Name the blood parasite species.
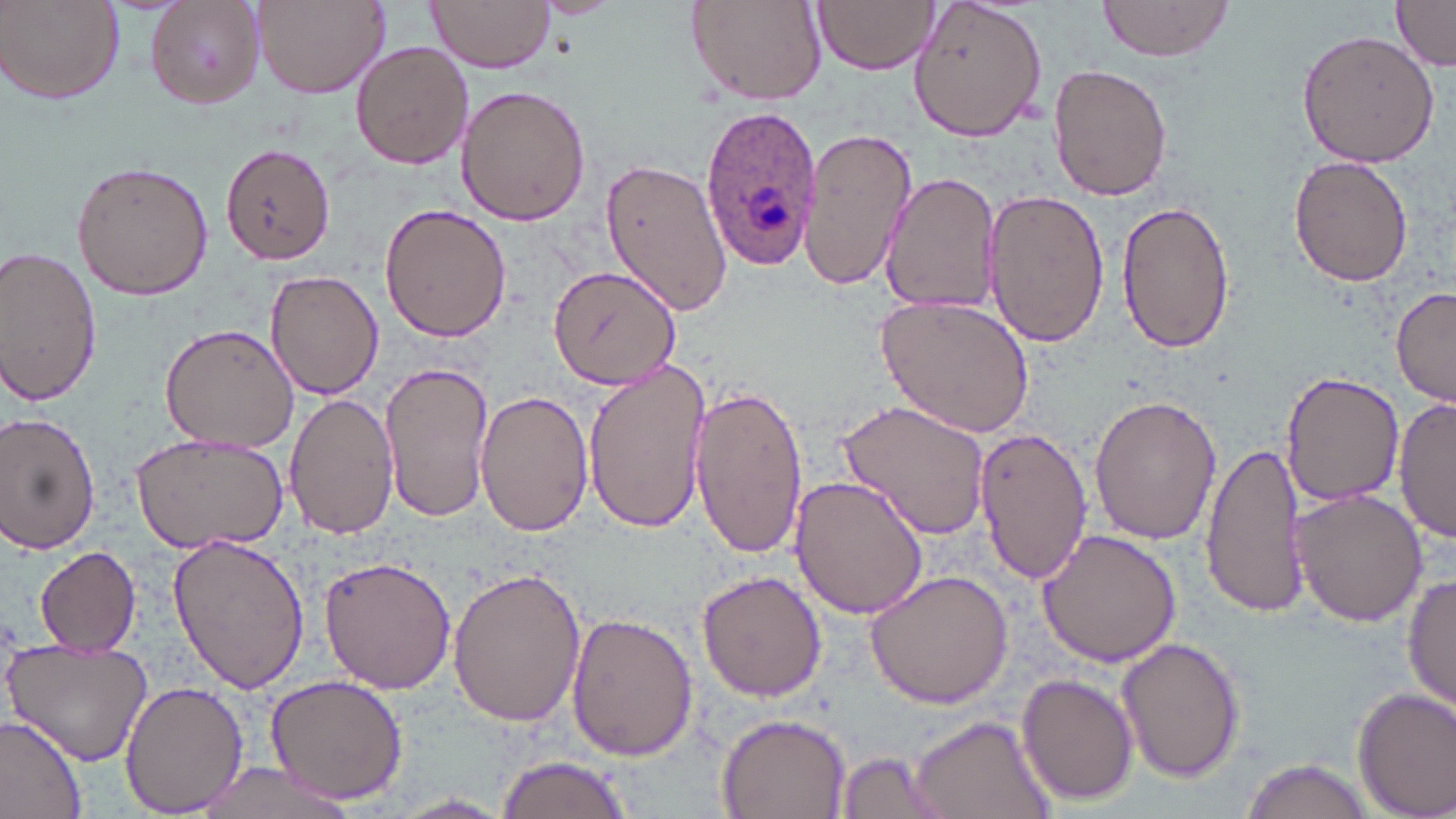

Plasmodium ovale.

Approximate bounding boxes as [x1, y1, x2, y2] in pixels. Uninfected red blood cell locations: [2, 0, 125, 106], [146, 0, 267, 109], [251, 0, 390, 97], [428, 0, 555, 73], [685, 0, 828, 107], [813, 0, 939, 75], [906, 0, 1048, 141], [1094, 0, 1239, 63], [1391, 0, 1456, 71], [1297, 28, 1439, 169], [351, 41, 474, 171], [1049, 63, 1172, 201], [455, 85, 591, 225], [800, 129, 914, 291], [221, 143, 333, 264], [597, 153, 732, 317], [1288, 156, 1416, 286], [69, 159, 213, 301], [879, 170, 1000, 315], [982, 187, 1110, 351], [1114, 195, 1235, 355], [379, 201, 512, 343], [0, 248, 102, 405], [547, 263, 680, 391], [265, 269, 384, 401], [1391, 286, 1455, 409], [875, 291, 1037, 439], [158, 322, 300, 453], [584, 357, 712, 536], [378, 358, 493, 524], [1281, 371, 1404, 509], [690, 379, 807, 561], [476, 389, 595, 535], [283, 391, 398, 540], [1088, 394, 1222, 546], [836, 397, 991, 540], [1393, 398, 1455, 545], [0, 412, 102, 554], [972, 427, 1091, 583], [129, 431, 290, 554], [1204, 441, 1306, 621], [791, 473, 930, 619], [1289, 488, 1429, 628], [1035, 529, 1183, 667], [168, 532, 311, 695], [32, 544, 142, 656], [318, 555, 456, 695], [864, 567, 1017, 709], [447, 568, 586, 725], [697, 570, 826, 701], [1402, 571, 1455, 719], [566, 612, 699, 762], [1116, 638, 1247, 781], [5, 639, 154, 766], [263, 672, 409, 805], [1016, 672, 1139, 805], [119, 681, 248, 815], [1353, 686, 1456, 818], [716, 710, 853, 819], [905, 714, 1057, 819], [0, 717, 88, 818], [835, 749, 948, 818], [495, 751, 635, 819], [1239, 757, 1376, 819], [182, 762, 368, 819], [389, 793, 515, 818]. Plasmodium ovale-infected red blood cell locations: [697, 104, 823, 277]. Thin blood smear. One field of a larger specimen. 1000x magnification. May-Grünwald-Giemsa-stained preparation. Image is 1456×819 pixels. Optical microscopy.